Locate every blood parasite and identify its species.
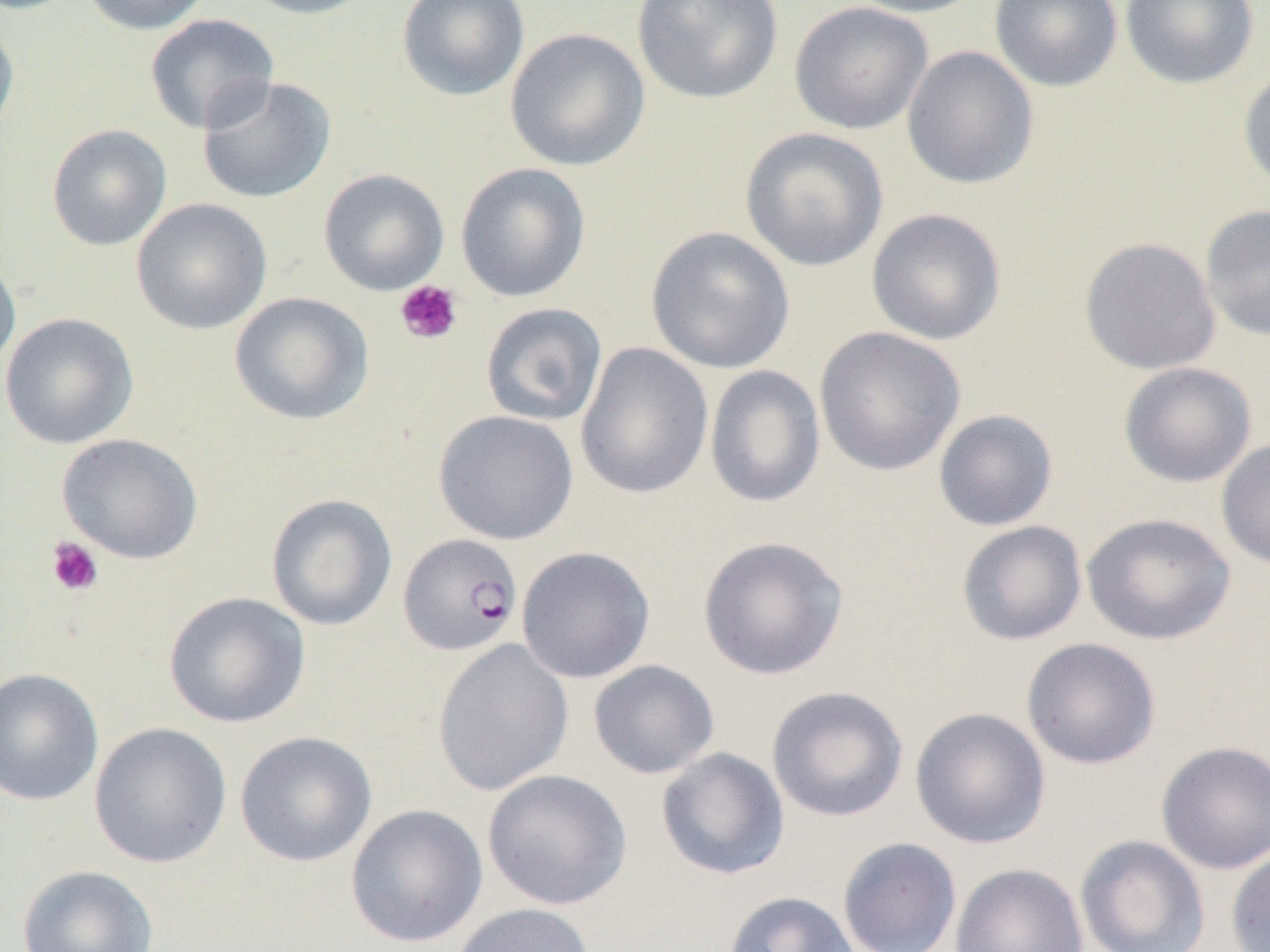
Approximate bounding boxes as [x1, y1, x2, y2] in pixels.
Plasmodium falciparum-infected red blood cells: [398, 533, 523, 656].
No Plasmodium ovale, Plasmodium malariae, Plasmodium vivax, Babesia divergens, or Trypanosoma brucei observed.

Summary:
  - Platelet locations: [394, 280, 463, 346], [46, 537, 103, 597]
  - Uninfected red blood cell locations: [80, 0, 214, 35], [237, 0, 379, 19], [396, 0, 530, 102], [631, 0, 783, 105], [842, 0, 988, 18], [989, 0, 1123, 92], [1119, 0, 1260, 90], [789, 1, 933, 135], [145, 14, 279, 134], [0, 17, 20, 142], [504, 27, 650, 171], [901, 45, 1039, 190], [1237, 65, 1270, 193], [196, 76, 336, 205], [46, 124, 172, 251], [740, 127, 889, 272], [455, 162, 591, 302], [318, 168, 450, 296], [131, 198, 272, 335], [1200, 204, 1270, 342], [866, 208, 1007, 346], [645, 226, 795, 375], [1079, 237, 1222, 375], [0, 247, 21, 376], [228, 291, 374, 426], [480, 302, 608, 427], [0, 312, 139, 449], [814, 326, 965, 477], [574, 342, 714, 500], [1118, 361, 1257, 488], [704, 365, 826, 509], [933, 409, 1058, 531], [433, 410, 578, 545], [57, 433, 204, 564], [1216, 440, 1270, 571], [265, 493, 398, 631], [1081, 512, 1236, 645], [955, 520, 1087, 646], [696, 535, 849, 680], [516, 546, 656, 684], [163, 591, 311, 729], [1021, 637, 1161, 770], [431, 638, 574, 796], [588, 659, 720, 779], [0, 667, 104, 806], [766, 685, 909, 822], [910, 707, 1052, 849], [88, 722, 233, 869], [234, 731, 378, 867], [1155, 741, 1270, 874], [656, 747, 790, 880], [482, 769, 632, 910], [345, 804, 488, 948], [1075, 834, 1210, 952], [837, 837, 962, 952], [1226, 845, 1270, 952], [950, 862, 1089, 952], [17, 864, 159, 952], [722, 891, 861, 952], [449, 902, 596, 952]
  - Slide-level diagnosis: Plasmodium falciparum
  - Image size: 1270×952 pixels
  - Preparation: thin blood smear
  - Magnification: 1000x
  - Modality: optical microscopy
  - Field of view: one of a larger specimen